Classify this cell by malaria status.
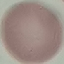

Uninfected.

Summary:
  - Capture: smartphone camera at the microscope eyepiece
  - Image type: cell patch, automatically extracted from a larger field of view and resized to 64 × 64 pixels
  - Stain: Giemsa
  - Preparation: thin blood film